Identify the parasite.
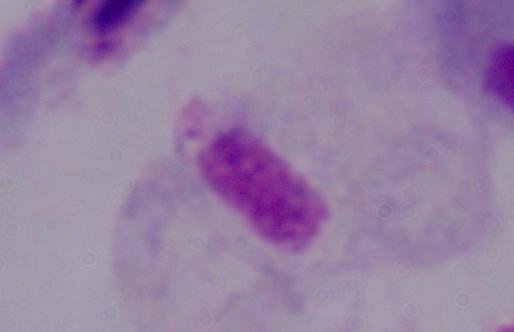

This is a trichomonad.

Captured at 1000x magnification. Photomicrograph.